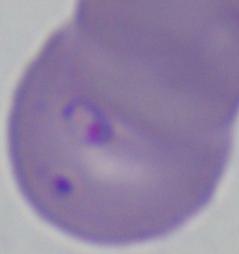 Photomicrograph. A Babesia parasite is seen. Captured at 1000x magnification.